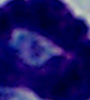

Photomicrograph. 1000x magnification. A white blood cell is seen.